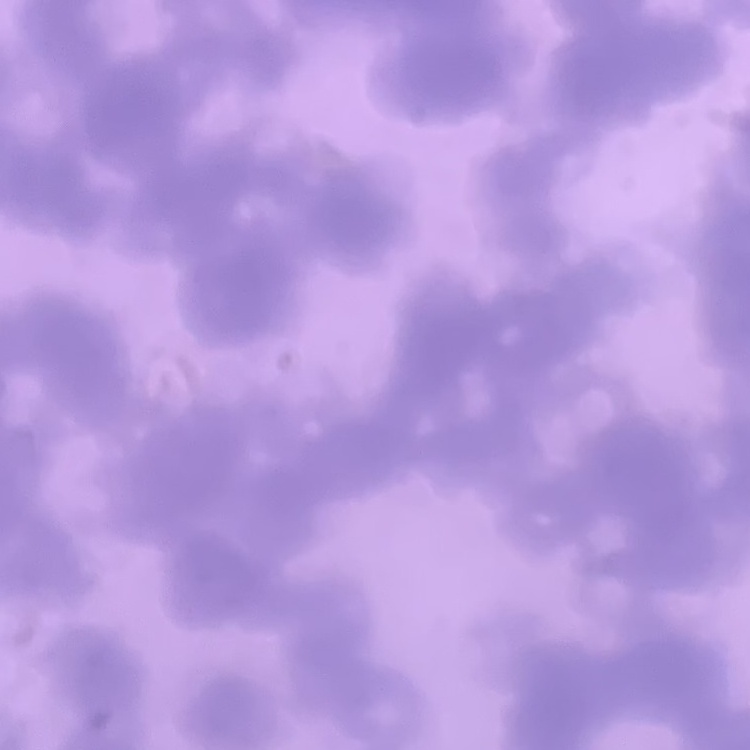
Summary:
  - Red blood cell morphology: rouleaux formation
  - Preparation: thin blood smear
  - Image type: one tile cut from a larger photomicrograph
  - Stain: Field's or Giemsa